Name the blood parasite species.
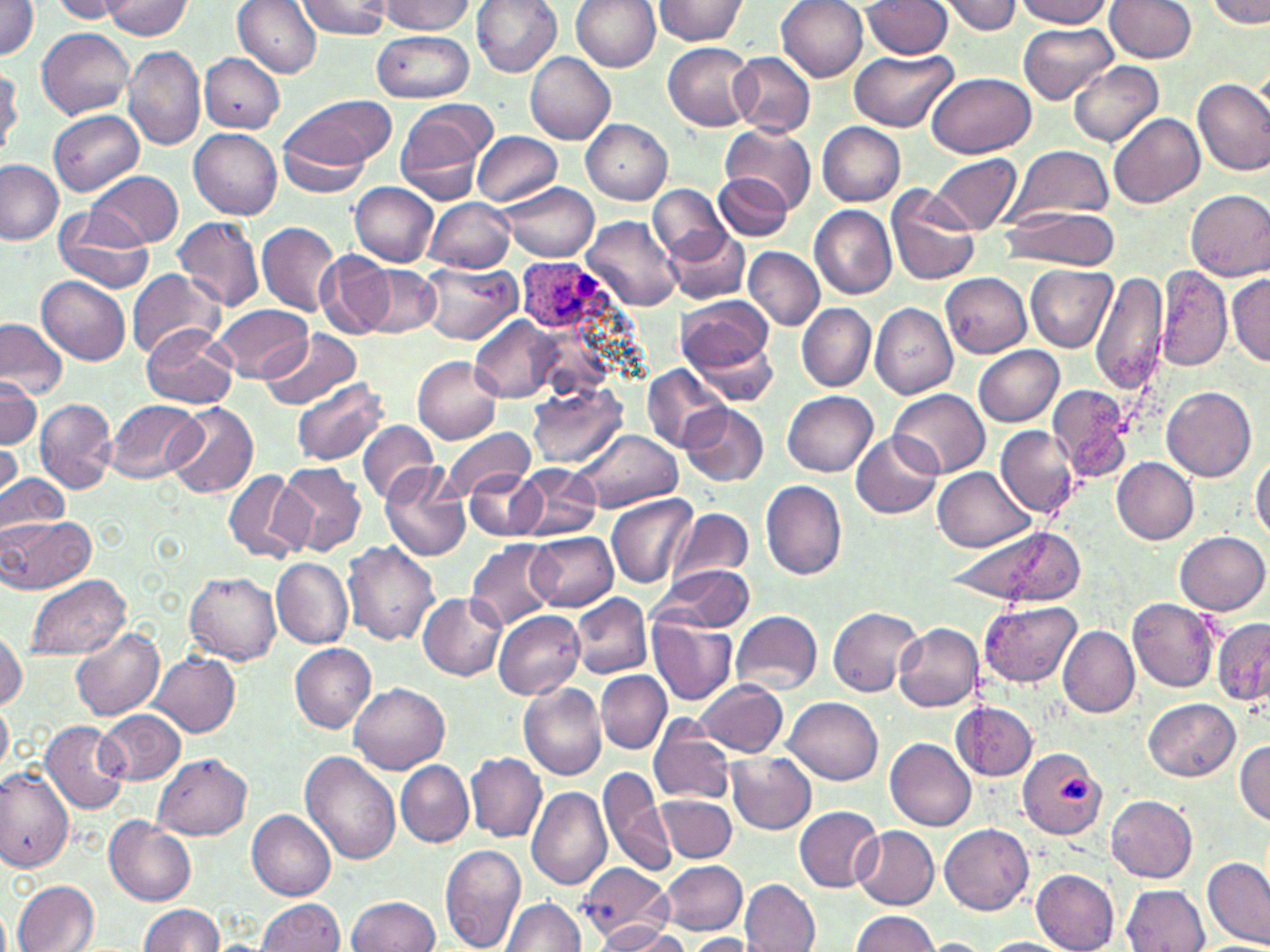

Plasmodium ovale.

Approximate bounding boxes as (x1,y1)-(x2,y2) corner pairs in pixels. Platelet locations: (1058,776)-(1091,805). Uninfected red blood cell locations: (0,0)-(38,61), (53,0)-(126,21), (299,0)-(390,38), (377,0)-(473,34), (471,0)-(561,75), (569,0)-(659,71), (656,0)-(750,45), (776,0)-(869,81), (941,0)-(1023,35), (1015,0)-(1113,27), (101,1)-(194,39), (234,1)-(322,77), (862,1)-(952,59), (1104,1)-(1196,64), (1206,1)-(1270,28), (1018,22)-(1118,104), (37,27)-(135,119), (372,31)-(473,104), (663,42)-(757,131), (123,45)-(205,151), (850,48)-(955,132), (727,51)-(816,136), (525,52)-(616,145), (199,53)-(283,133), (1069,61)-(1163,147), (1,66)-(22,153), (924,71)-(1037,158), (1193,75)-(1270,178), (289,94)-(393,167), (398,102)-(492,198), (48,110)-(145,196), (1109,112)-(1205,209), (278,115)-(374,198), (582,118)-(672,204), (817,122)-(906,205), (720,124)-(816,215), (189,129)-(282,218), (472,130)-(561,207), (1007,145)-(1114,224), (929,154)-(1023,236), (0,159)-(63,245), (89,170)-(183,248), (714,172)-(793,241), (498,181)-(600,262), (350,182)-(438,265), (885,184)-(980,285), (648,185)-(731,265), (1186,188)-(1270,280), (426,198)-(515,272), (52,205)-(157,297), (809,205)-(897,299), (999,205)-(1119,270), (172,216)-(264,311), (583,216)-(683,311), (256,221)-(339,315), (664,227)-(751,305), (745,247)-(825,330), (316,251)-(395,338), (419,261)-(519,343), (366,264)-(440,338), (1155,264)-(1231,373), (1027,265)-(1115,351), (128,270)-(224,359), (1090,271)-(1168,393), (941,273)-(1033,357), (1227,273)-(1270,368), (39,275)-(130,364), (677,295)-(776,379), (870,302)-(957,401), (797,303)-(876,390), (212,304)-(314,382), (470,315)-(563,403), (0,317)-(69,402), (140,327)-(237,408), (260,327)-(360,411), (689,335)-(781,407), (975,346)-(1064,427), (412,356)-(501,444), (643,366)-(729,452), (0,374)-(40,451), (293,377)-(389,466), (1048,383)-(1133,479), (527,384)-(626,468), (1163,386)-(1258,483), (891,388)-(989,478), (783,391)-(878,477), (35,398)-(116,494), (107,400)-(201,484), (166,401)-(257,498), (681,402)-(768,486), (359,420)-(438,503), (441,425)-(533,502), (996,426)-(1081,517), (573,429)-(682,512), (850,429)-(943,519), (0,439)-(22,502), (1250,449)-(1270,546), (1111,457)-(1199,544), (276,461)-(368,556), (379,461)-(469,562), (513,462)-(602,541), (464,467)-(544,539), (931,468)-(1037,551), (0,471)-(68,538), (224,471)-(305,566), (760,479)-(847,580), (606,493)-(698,590), (667,508)-(753,588), (4,516)-(95,592), (943,523)-(1089,607), (1176,530)-(1270,616), (528,531)-(619,610), (467,539)-(560,633), (343,540)-(440,644), (270,557)-(352,648), (653,565)-(757,632), (185,572)-(281,663), (26,575)-(130,661), (419,593)-(506,680), (570,593)-(653,678), (1128,597)-(1218,691), (979,600)-(1081,687), (828,607)-(921,697), (493,610)-(585,699), (731,611)-(822,693), (1212,617)-(1270,707), (646,619)-(737,703), (895,623)-(984,712), (71,626)-(163,720), (1060,626)-(1140,718), (0,627)-(24,712), (290,643)-(376,732), (149,652)-(240,736), (597,670)-(670,752), (695,680)-(787,757), (349,682)-(449,774), (519,682)-(606,782), (785,696)-(881,784), (1145,698)-(1240,781), (0,700)-(11,777), (952,701)-(1038,780), (96,709)-(184,785), (648,718)-(736,807), (39,720)-(129,815), (885,739)-(976,831), (1235,740)-(1270,825), (1017,748)-(1105,840), (301,751)-(403,865), (466,752)-(546,842), (726,752)-(816,834), (153,754)-(251,840), (396,760)-(474,846), (598,767)-(674,877), (0,768)-(74,872), (526,785)-(612,891), (657,793)-(736,863), (1105,794)-(1197,881), (794,806)-(882,892), (246,808)-(335,900), (105,816)-(197,905), (940,823)-(1034,915), (852,827)-(939,909), (438,843)-(527,952), (1201,855)-(1270,948), (658,859)-(748,935), (579,864)-(668,942), (1030,869)-(1121,952), (665,872)-(821,945), (742,879)-(820,952), (13,880)-(100,951), (1123,885)-(1210,952), (346,895)-(439,952), (502,898)-(588,952), (255,899)-(344,952), (138,903)-(225,952), (850,911)-(940,952), (590,921)-(684,951), (684,934)-(757,951), (980,937)-(1075,952), (924,939)-(988,952). Plasmodium ovale-infected red blood cell locations: (519,259)-(611,329). Thin blood smear. One field of a larger specimen. Captured at 1000x magnification. May-Grünwald-Giemsa stain. Image is 1270×952 pixels. Optical microscopy.